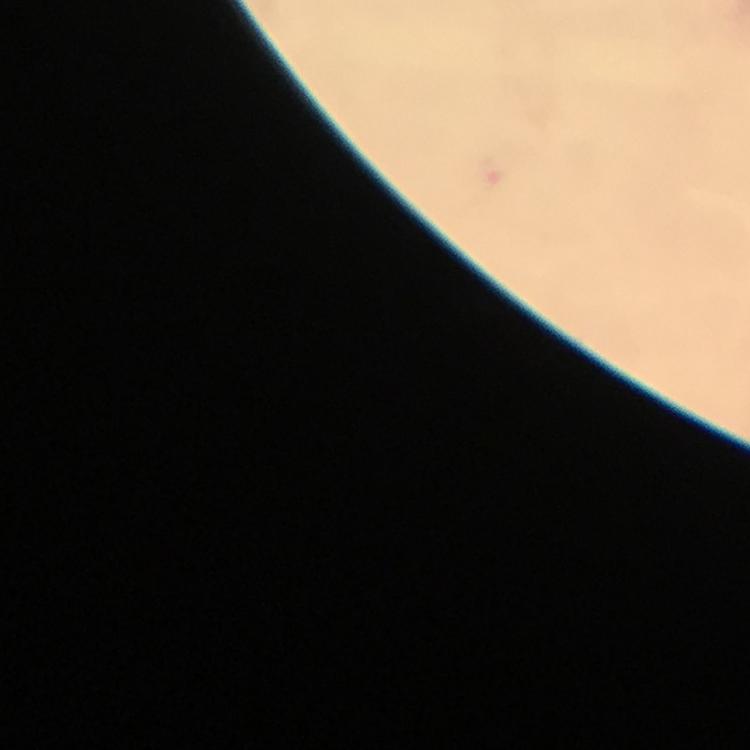

magnification: 100x
preparation: thick blood smear
cropped_from: a single field of view
context: from a diagnostic examination for malaria
stain: Giemsa
capture: smartphone camera through the microscope
immersion_oil: used
image_size: 750×750 pixels
malaria_parasite_locations: 'approximate centers as (x, y) in pixels: (497, 168)'